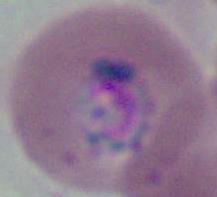

identification = Plasmodium
modality = micrograph
magnification = 400x or 1000x